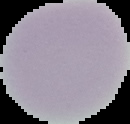 Image is 130×124 pixels. Segmented cell region on a black background. Malaria status: uninfected. From a thin blood film.